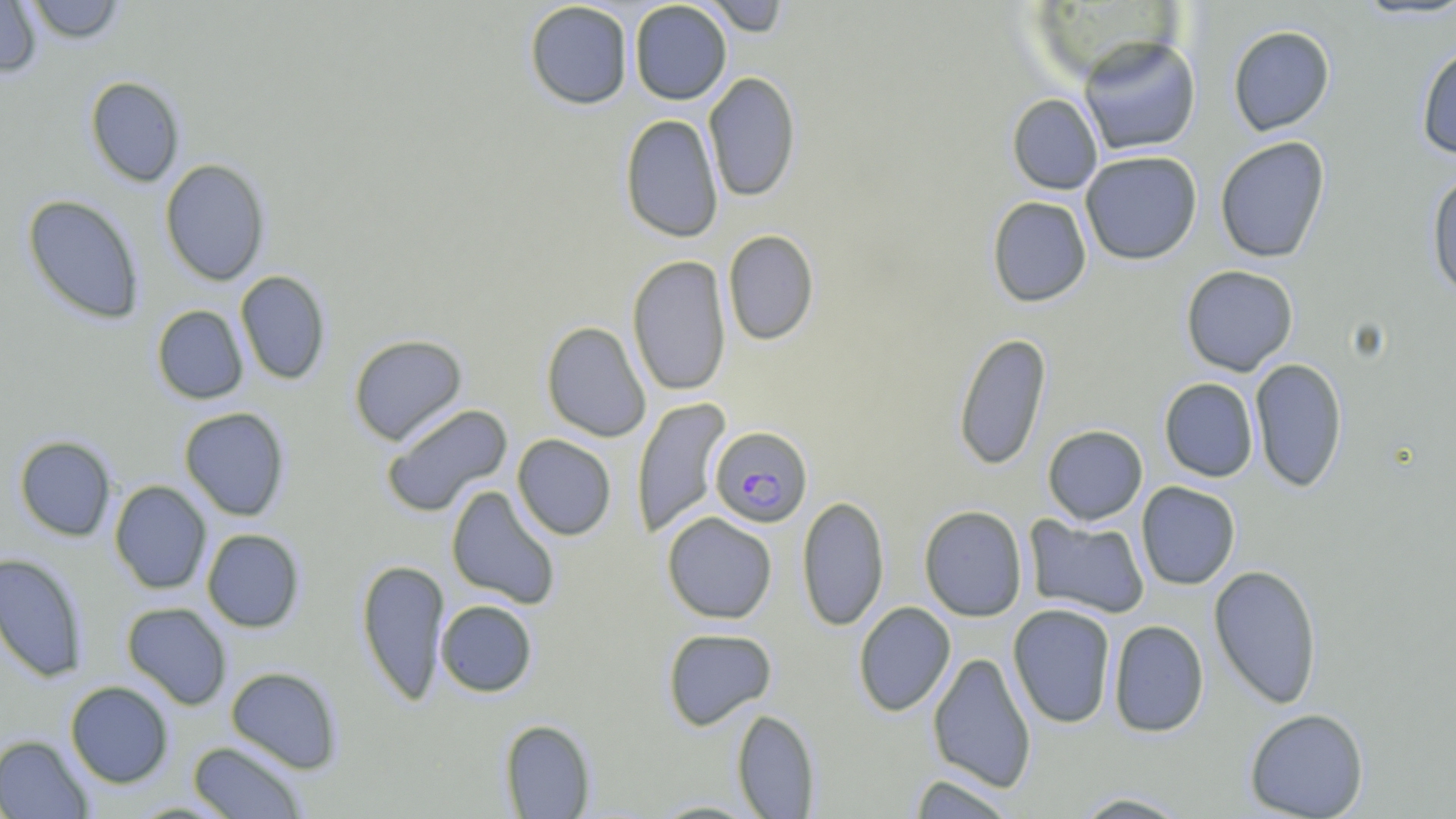
Summary:
  - Coordinate format: approximate bounding boxes as [x1, y1, x2, y2] in pixels
  - Plasmodium falciparum-infected red blood cell locations: [709, 426, 813, 528]
  - Uninfected red blood cell locations: [0, 0, 42, 78], [24, 0, 126, 44], [700, 0, 791, 37], [524, 1, 633, 110], [629, 1, 732, 105], [1352, 1, 1456, 22], [1227, 25, 1335, 136], [1078, 36, 1201, 156], [1415, 41, 1456, 159], [703, 71, 801, 202], [85, 76, 185, 187], [1007, 93, 1102, 195], [619, 113, 723, 242], [1214, 136, 1330, 263], [1080, 150, 1203, 265], [159, 158, 271, 286], [1426, 168, 1456, 300], [22, 193, 145, 324], [987, 196, 1092, 307], [722, 229, 819, 346], [627, 254, 731, 396], [1180, 265, 1299, 376], [235, 270, 331, 385], [152, 305, 249, 404], [541, 321, 651, 442], [953, 332, 1052, 470], [348, 334, 467, 446], [1249, 357, 1348, 493], [1158, 378, 1259, 482], [632, 397, 731, 539], [381, 403, 513, 518], [179, 407, 291, 521], [1042, 425, 1148, 525], [512, 434, 617, 540], [14, 435, 117, 542], [109, 480, 212, 594], [1136, 482, 1241, 590], [446, 485, 561, 609], [797, 495, 889, 631], [919, 505, 1028, 622], [661, 512, 778, 624], [1024, 516, 1150, 619], [202, 528, 305, 632], [0, 553, 89, 682], [355, 558, 451, 706], [1208, 564, 1323, 709], [435, 600, 538, 697], [122, 602, 233, 710], [853, 602, 956, 717], [1007, 603, 1117, 728], [1108, 620, 1209, 738], [662, 627, 777, 730], [928, 651, 1036, 793], [226, 666, 343, 773], [65, 681, 174, 788], [732, 708, 820, 818], [1244, 708, 1369, 819], [499, 719, 596, 818], [0, 734, 94, 819], [188, 740, 308, 818], [906, 773, 1020, 818], [1070, 791, 1194, 817], [648, 800, 766, 818]
  - Slide-level diagnosis: Plasmodium falciparum
  - Modality: light microscopy
  - Field of view: single
  - Image size: 1456×819 pixels
  - Stain: May-Grünwald-Giemsa
  - Magnification: 1000x
  - Preparation: thin blood film